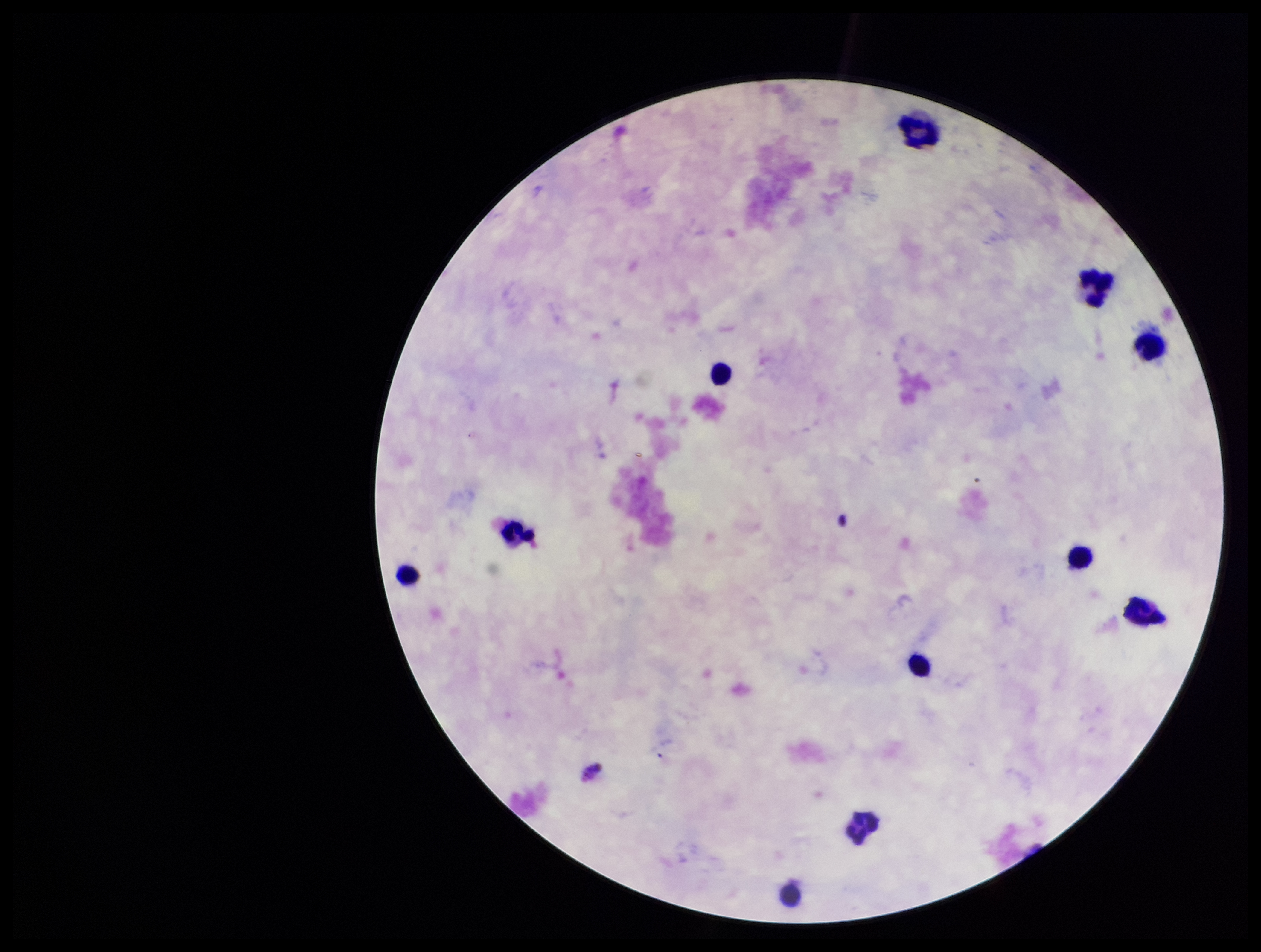
One field from this slide. Leukocyte count: 10. Plasmodium parasites: none seen. Patient malaria status: negative. Giemsa stain. Parasite count: 0. Preparation: thick smear. Photographed through the microscope eyepiece with a smartphone camera. Image is 1261×952 pixels.